Draw a bounding box around every parasitised red blood cell, every trophozoite, every gametocyte, every leukocyte, and every artifact (platelet-like body, stain precipitate, or debris).
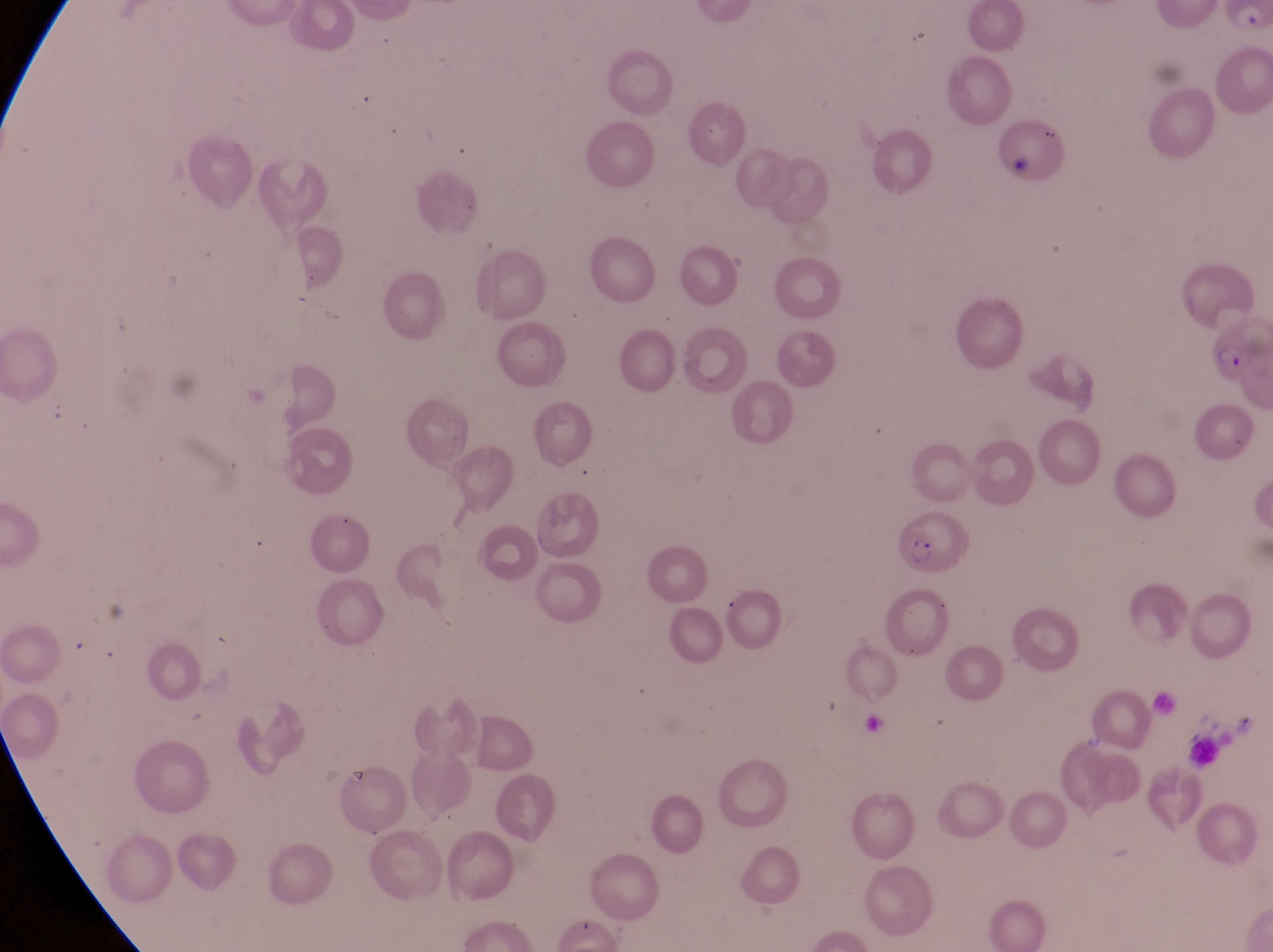

Approximate bounding boxes as left top right bottom in pixels.
Parasitised red blood cells: 1199 314 1272 384; 896 505 973 575.
No leukocytes observed.
Artifacts (platelet-like body, stain precipitate, or debris): 998 118 1033 178.

field of view = single
magnification = 1000x
country = Uganda
preparation = thin blood smear
image size = 1273×952 pixels
capture = smartphone photograph through the eyepiece of an Olympus CX-23 microscope